Assess this cell for malaria.
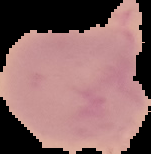

Uninfected.

image type = cell region segmented out of the field of view; surrounding area masked to black
preparation = thin blood smear
image size = 151×154 pixels